Name the parasite shown.
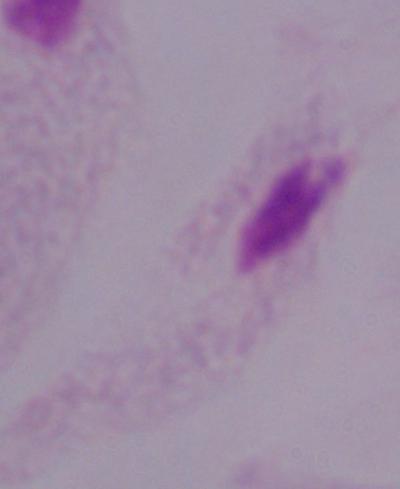
A trichomonad.

{
  "modality": "micrograph",
  "magnification": "1000x"
}